Give the extent of all Plasmodium malariae-infected red blood cells.
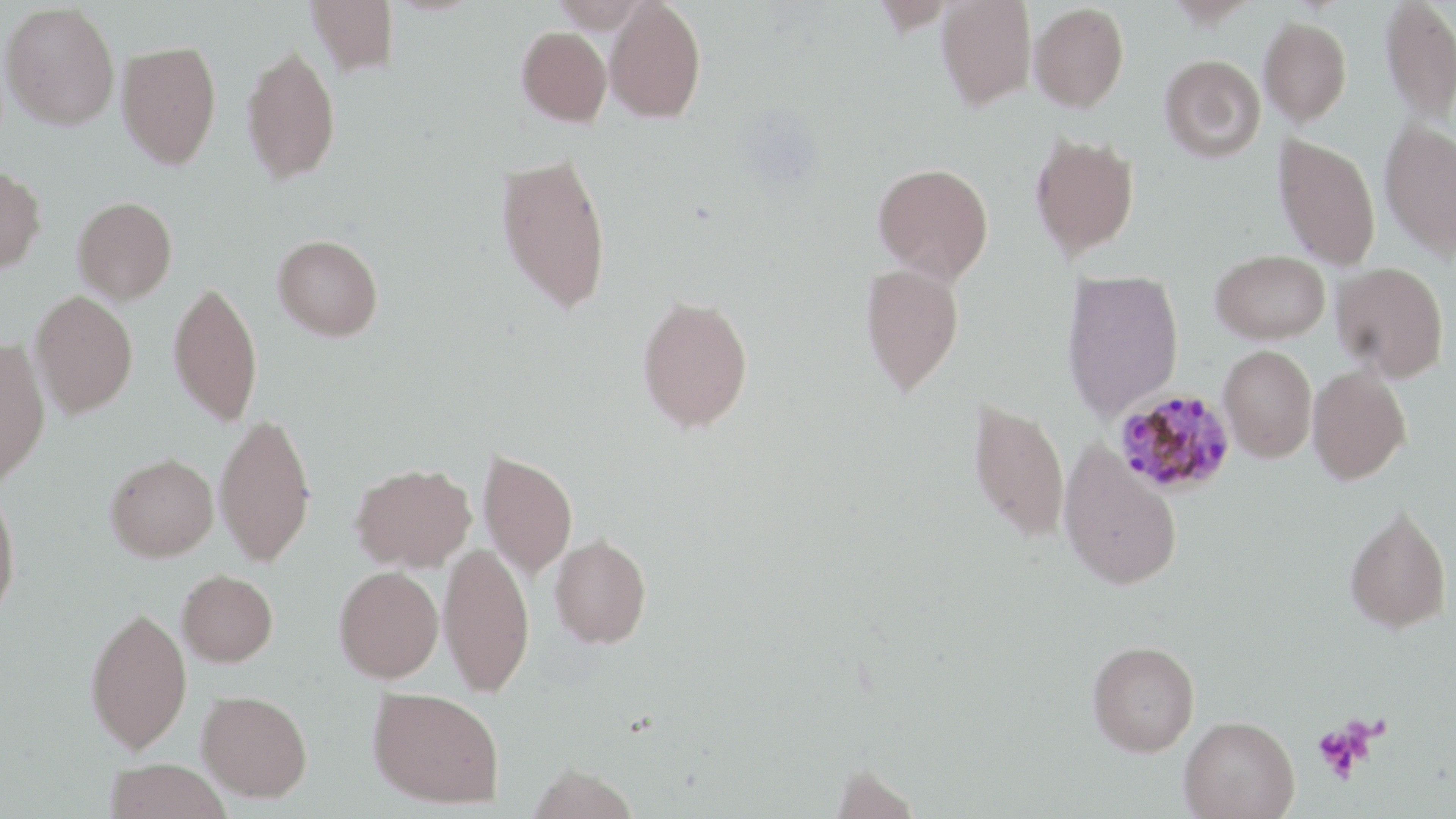
Approximate bounding boxes as (x1,y1)-(x2,y2) corner pairs in pixels.
Plasmodium malariae-infected red blood cells: (1114,388)-(1237,496).

Platelet locations: (1313,720)-(1374,781). Uninfected red blood cell locations: (306,0)-(398,75), (604,0)-(706,123), (936,0)-(1037,110), (1380,0)-(1456,124), (1,2)-(120,130), (1029,2)-(1129,111), (1259,16)-(1352,125), (516,26)-(611,126), (116,40)-(222,169), (240,43)-(340,184), (1160,54)-(1265,162), (1380,120)-(1456,261), (1029,132)-(1139,260), (1273,133)-(1381,271), (496,151)-(613,315), (873,162)-(994,283), (0,166)-(46,275), (72,197)-(177,304), (273,234)-(384,341), (1210,249)-(1330,343), (860,262)-(965,396), (1332,262)-(1449,382), (1061,270)-(1184,421), (168,279)-(263,426), (30,290)-(138,418), (637,294)-(753,432), (0,337)-(50,488), (1218,345)-(1317,462), (1308,364)-(1411,484), (968,398)-(1070,542), (214,410)-(317,567), (1058,441)-(1184,590), (479,451)-(577,579), (105,453)-(218,561), (351,462)-(476,572), (0,489)-(22,619), (1344,503)-(1451,633), (550,534)-(651,648), (439,541)-(534,697), (334,566)-(443,683), (177,570)-(279,667), (85,605)-(192,754), (1087,641)-(1199,756), (368,687)-(504,808), (197,690)-(313,802), (1179,715)-(1299,819), (105,759)-(231,819), (527,764)-(640,819), (831,765)-(922,818). Slide-level diagnosis: Plasmodium malariae. Thin blood smear. Image is 1456×819 pixels. May-Grünwald-Giemsa stain. Single field of view. Captured at 1000x magnification. Optical microscopy.